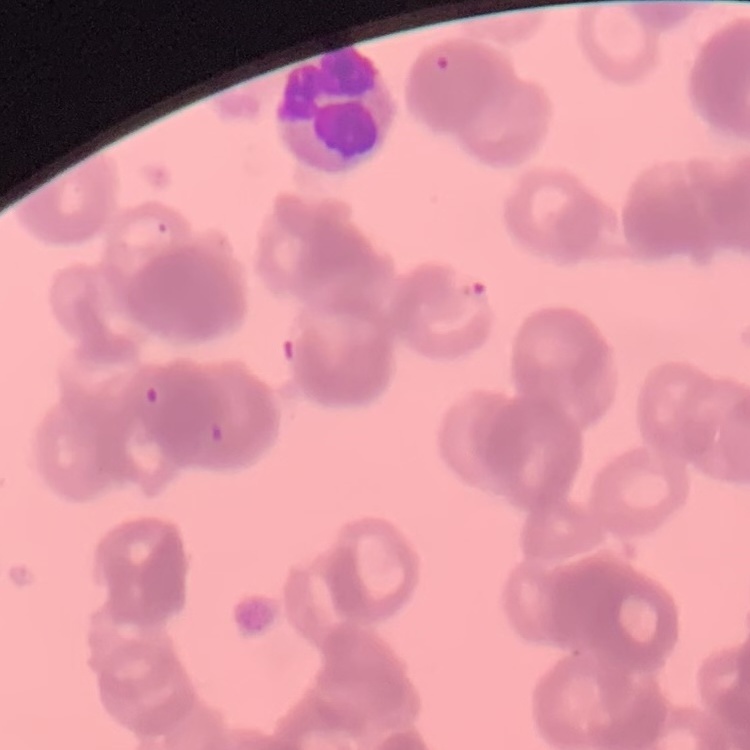
Summary:
  - Red blood cell morphology: rouleaux formation
  - Stain: Field's or Giemsa
  - Image type: one tile cut from a larger photomicrograph
  - Preparation: thin blood film